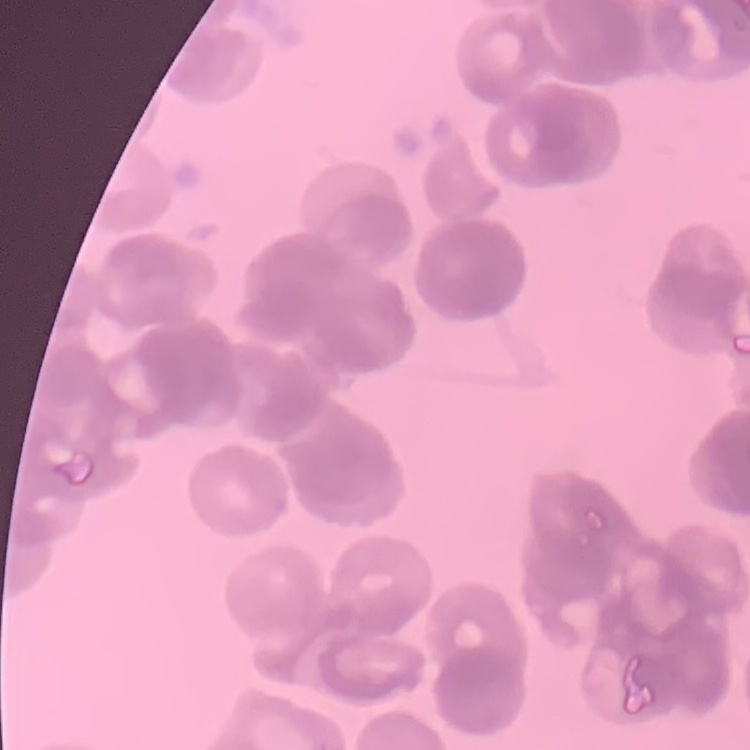
red_blood_cell_morphology: rouleaux formation
stain: Field's or Giemsa
image_type: square crop of a larger photomicrograph
preparation: thin blood film